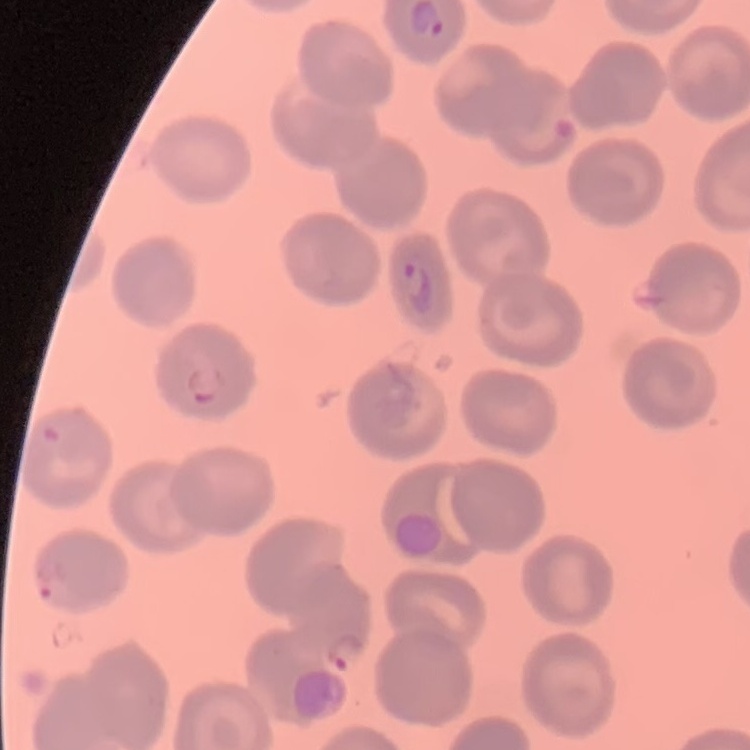
The erythrocytes exhibit no rouleaux formation. Stained with either Field's or Giemsa. Square crop of a larger photomicrograph. Thin blood smear.